State which cell type is depicted.
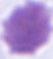
This is an erythrocyte.

1000x magnification. Micrograph.